Identify the parasite.
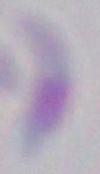
This is Toxoplasma gondii.

Summary:
  - Magnification: 1000x
  - Modality: photomicrograph